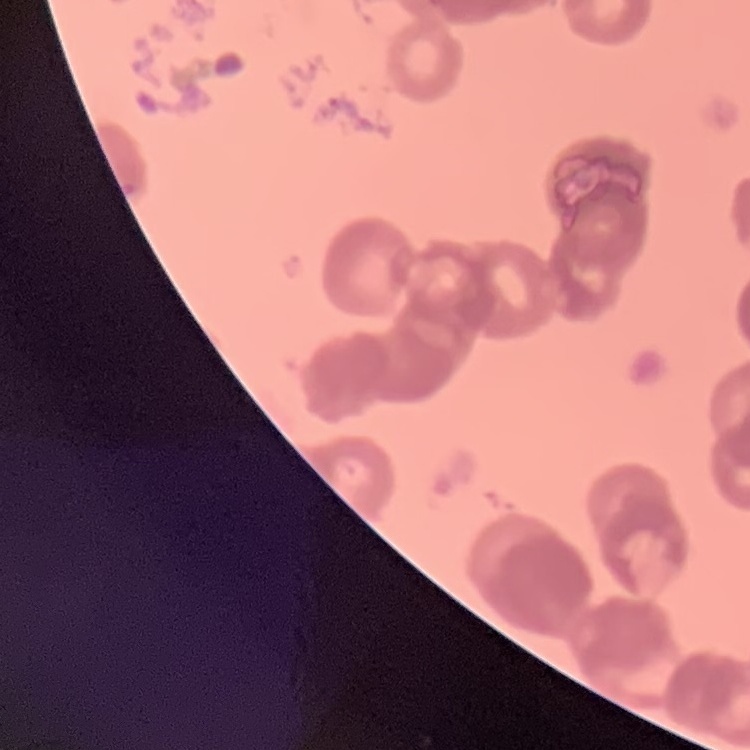 The red blood cells exhibit rouleaux formation. Field's or Giemsa stain. Thin blood film. Square crop of a larger photomicrograph.